Give the extent of all Plasmodium ovale-infected red blood cells.
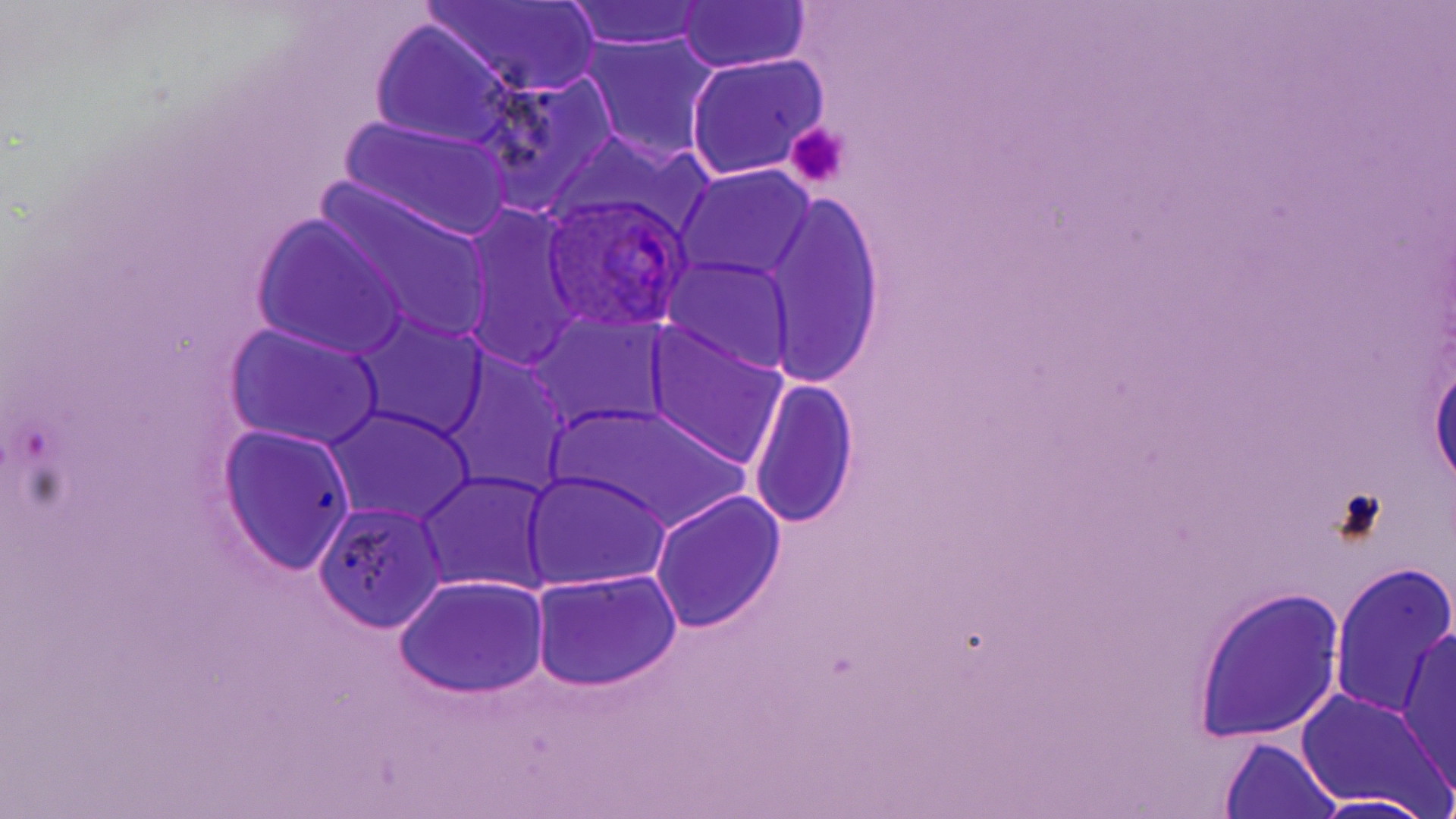

Approximate bounding boxes as (x1, y1, x2, y2) in pixels.
Plasmodium ovale-infected red blood cells: (539, 193, 693, 335).

Platelet locations: (785, 121, 851, 192). Uninfected red blood cell locations: (562, 2, 711, 52), (673, 2, 812, 74), (425, 3, 601, 96), (369, 21, 518, 151), (577, 34, 723, 166), (684, 53, 827, 182), (468, 72, 617, 211), (340, 115, 515, 242), (552, 130, 710, 239), (674, 165, 817, 285), (319, 185, 494, 347), (765, 192, 888, 391), (459, 203, 586, 373), (253, 217, 408, 361), (660, 253, 798, 381), (526, 313, 672, 435), (348, 315, 490, 445), (643, 321, 790, 468), (225, 324, 385, 452), (1428, 348, 1456, 495), (439, 351, 573, 498), (749, 376, 857, 532), (552, 403, 751, 534), (325, 406, 475, 527), (218, 426, 356, 576), (416, 470, 556, 597), (521, 470, 673, 592), (650, 490, 787, 634), (315, 500, 448, 633), (1331, 560, 1454, 726), (531, 571, 682, 692), (395, 574, 549, 698), (1192, 587, 1345, 745), (1397, 628, 1456, 793), (1296, 689, 1452, 815), (1216, 736, 1343, 819), (1299, 792, 1441, 818). Slide-level diagnosis: Plasmodium ovale. Single field of view. Thin blood film. Image is 1456×819 pixels. May-Grünwald-Giemsa stain. Captured at 1000x magnification. Optical microscopy.